Describe the morphology of the red blood cells.
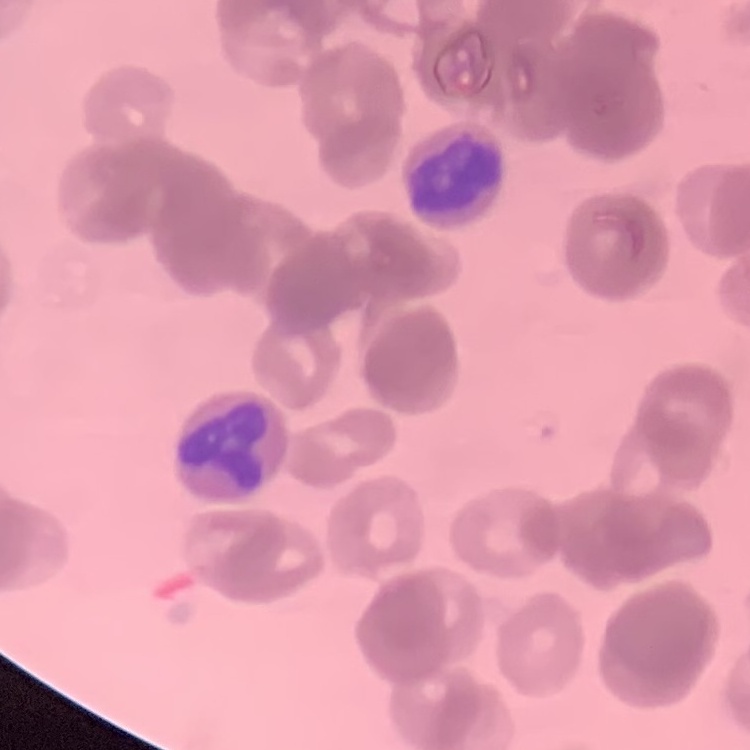

They show rouleaux formation.

Stained with either Field's or Giemsa. Square crop of a larger photomicrograph. Thin blood smear.